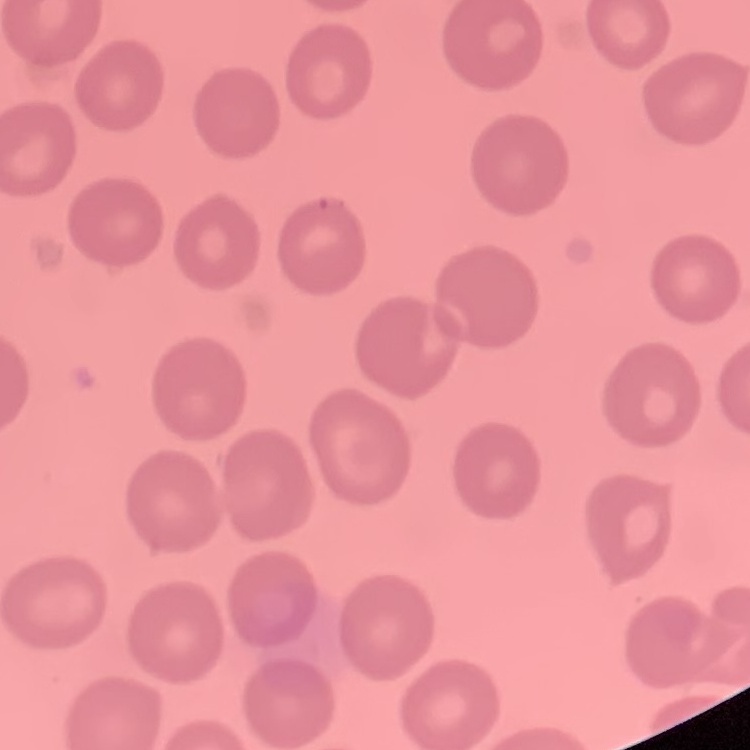
The red blood cells exhibit no rouleaux formation. Stained with either Field's or Giemsa. One tile cut from a larger photomicrograph. Thin peripheral smear.